Identify the cell.
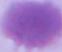
This is an erythrocyte.

Captured at 1000x magnification. Micrograph.